Assess this cell for malaria.
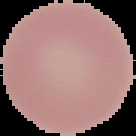

It is uninfected.

Image is 136×136 pixels. From a thin blood smear. Segmented cell region on a black background.